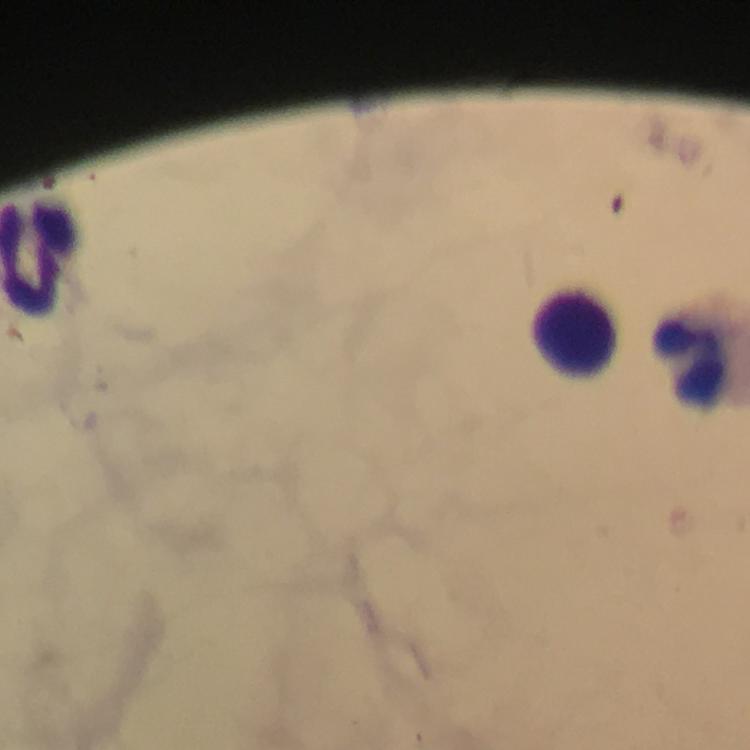
magnification: 100x
immersion_oil: applied
cropped_from: a single field of view
capture: smartphone photograph through a microscope
context: from a diagnostic examination for malaria
preparation: thick smear
leukocyte_locations: 'approximate centers as [x, y] in pixels: [577, 329]'
malaria_parasites: none detected
stain: Giemsa
image_size: 750×750 pixels